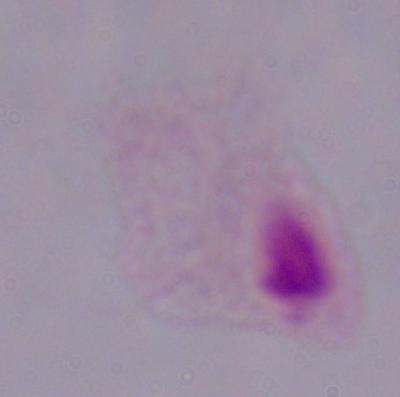

modality = photomicrograph
magnification = 1000x
identification = trichomonad